Describe the morphology of the erythrocytes.
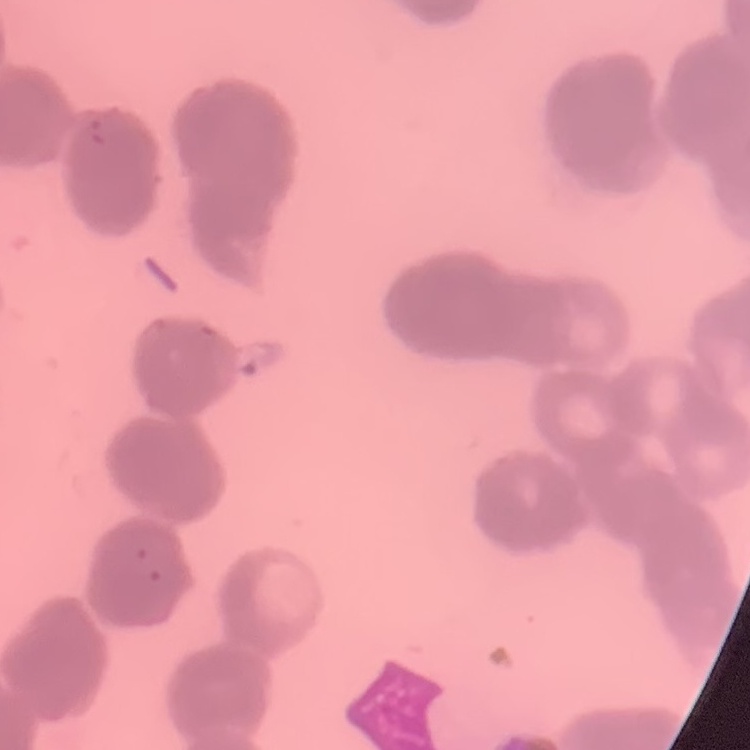
Rouleaux formation.

Thin blood film. Stained with either Field's or Giemsa. Square crop of a larger photomicrograph.